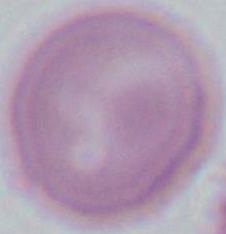

modality = photomicrograph
identification = red blood cell
magnification = 1000x